Identify the blood parasite species.
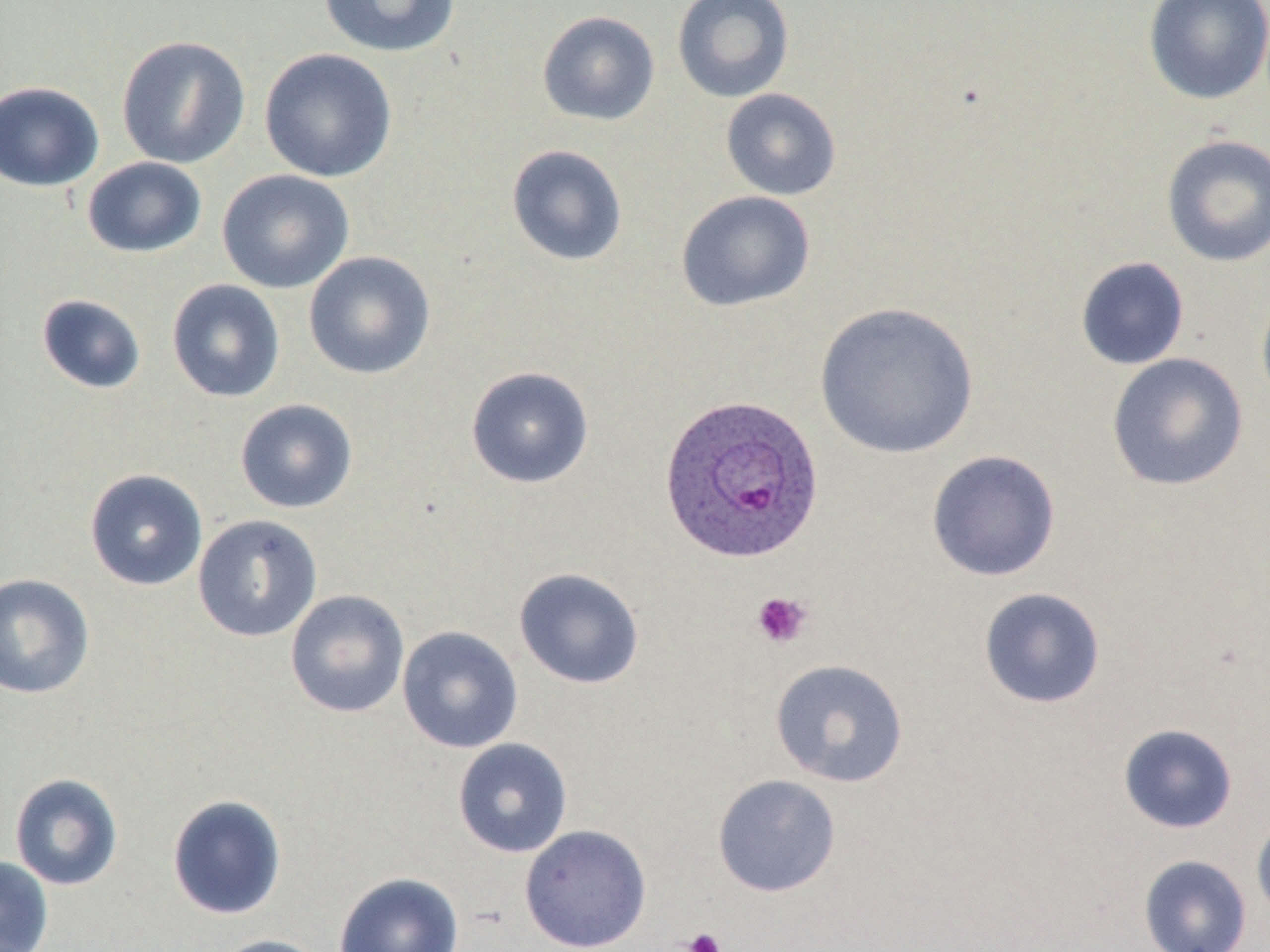
Plasmodium ovale.

preparation = thin blood film
platelet locations = approximate bounding boxes as (x1, y1, x2, y2) in pixels: (751, 591, 813, 649), (682, 928, 725, 952)
magnification = 1000x
Plasmodium ovale-infected red blood cell locations = approximate bounding boxes as (x1, y1, x2, y2) in pixels: (657, 393, 825, 564)
modality = optical microscopy
image size = 1270×952 pixels
uninfected red blood cell locations = approximate bounding boxes as (x1, y1, x2, y2) in pixels: (317, 0, 462, 58), (671, 0, 795, 103), (1143, 0, 1270, 106), (537, 11, 660, 126), (116, 35, 251, 169), (259, 48, 397, 183), (0, 81, 104, 192), (720, 88, 842, 201), (1160, 134, 1270, 268), (506, 144, 628, 266), (82, 157, 207, 259), (217, 169, 355, 294), (676, 191, 816, 312), (303, 251, 436, 380), (1075, 256, 1190, 370), (166, 278, 285, 403), (1255, 286, 1270, 412), (36, 294, 147, 394), (813, 301, 980, 459), (1106, 352, 1249, 491), (465, 366, 594, 489), (235, 398, 358, 513), (926, 450, 1061, 582), (84, 469, 208, 591), (192, 514, 322, 642), (513, 567, 645, 690), (0, 573, 95, 699), (978, 587, 1106, 709), (284, 589, 410, 718), (397, 625, 523, 754), (769, 658, 909, 788), (1118, 723, 1238, 834), (452, 738, 573, 857), (9, 772, 124, 890), (712, 773, 841, 898), (166, 794, 287, 920), (1251, 811, 1270, 925), (519, 823, 652, 952), (0, 855, 53, 952), (1138, 855, 1252, 952), (333, 872, 465, 952), (209, 934, 331, 952)
field of view = single
stain = May-Grünwald-Giemsa